Assess this cell for malaria.
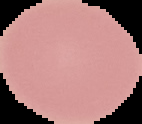

Uninfected.

From a thin blood smear. Image is 142×124 pixels. Segmented cell region on a black background.